Outline each uninfected red blood cell.
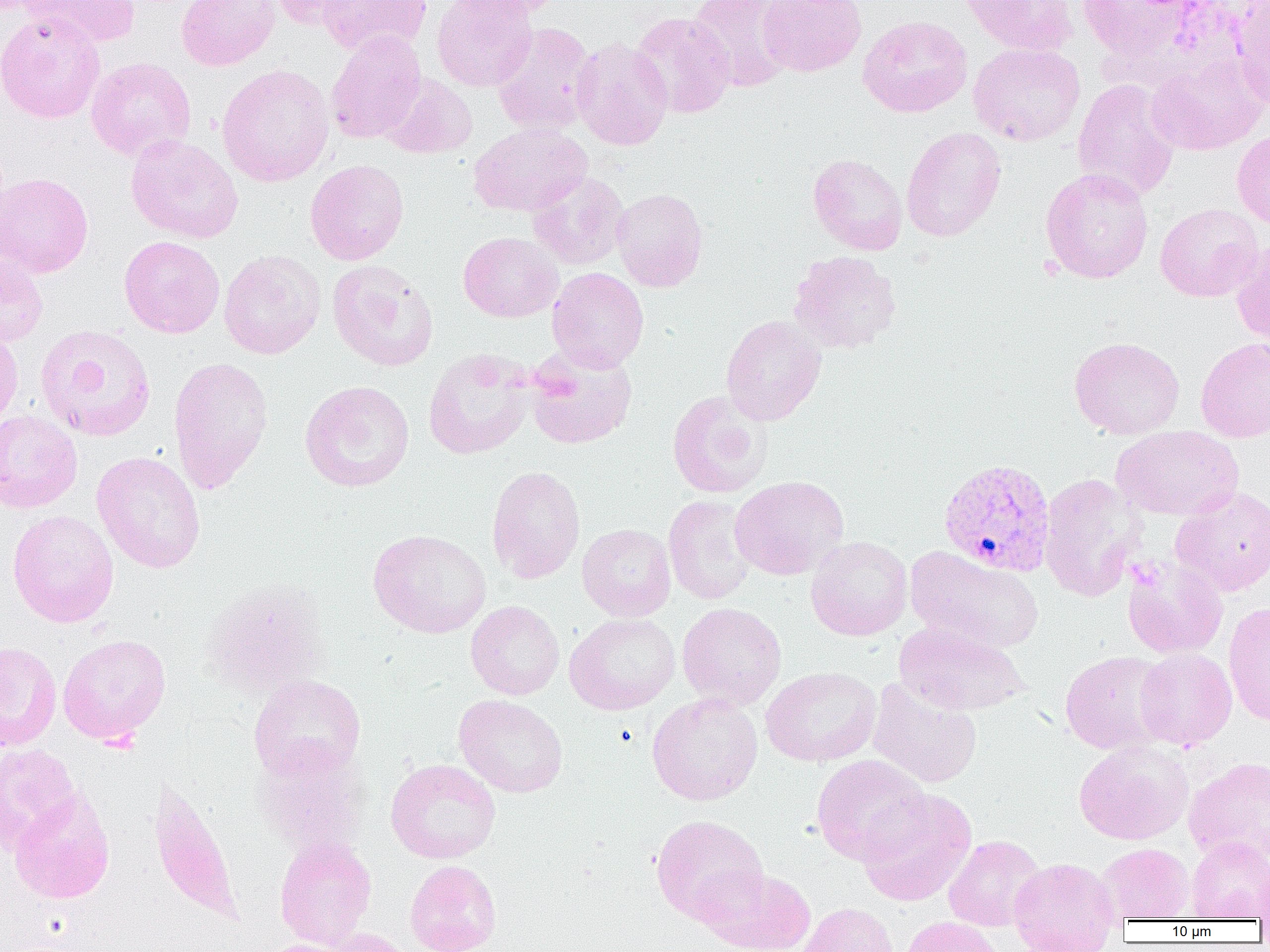
Approximate bounding boxes as [x1, y1, x2, y2] in pixels.
Uninfected red blood cells: [19, 0, 140, 48], [176, 0, 280, 71], [267, 0, 363, 30], [317, 0, 432, 57], [432, 0, 538, 92], [450, 0, 563, 21], [688, 0, 796, 92], [758, 0, 866, 77], [961, 0, 1077, 57], [1078, 0, 1197, 63], [1230, 1, 1270, 110], [629, 11, 736, 118], [0, 12, 106, 123], [858, 15, 973, 118], [492, 22, 597, 137], [326, 30, 426, 144], [571, 37, 673, 151], [968, 42, 1086, 146], [1145, 52, 1268, 155], [86, 57, 196, 161], [217, 64, 335, 187], [381, 73, 477, 159], [1072, 79, 1181, 201], [469, 123, 591, 216], [901, 127, 1006, 242], [1231, 128, 1270, 229], [125, 134, 244, 243], [808, 153, 908, 255], [305, 159, 409, 266], [1040, 167, 1154, 284], [527, 171, 630, 270], [0, 172, 94, 278], [611, 188, 709, 292], [1155, 203, 1264, 302], [458, 231, 563, 322], [119, 235, 225, 338], [1231, 239, 1270, 348], [0, 250, 48, 347], [219, 250, 326, 359], [788, 250, 901, 355], [327, 259, 439, 372], [547, 267, 649, 373], [720, 314, 826, 425], [0, 324, 23, 432], [34, 324, 156, 441], [1068, 336, 1185, 439], [1195, 336, 1270, 442], [526, 346, 637, 449], [422, 348, 536, 459], [168, 356, 273, 494], [299, 380, 415, 492], [666, 391, 773, 499], [0, 409, 82, 513], [1111, 427, 1243, 521], [91, 451, 206, 573], [486, 465, 586, 584], [1039, 473, 1145, 602], [730, 475, 849, 580], [1171, 486, 1270, 597], [663, 494, 758, 605], [7, 509, 119, 628], [577, 523, 676, 621], [367, 529, 492, 638], [805, 535, 913, 641], [905, 547, 1045, 654], [1122, 555, 1228, 659], [202, 580, 329, 698], [466, 600, 564, 700], [677, 602, 787, 710], [1223, 602, 1270, 725], [564, 613, 681, 715], [894, 622, 1030, 717], [58, 633, 171, 744], [0, 642, 61, 750], [1134, 648, 1237, 750], [1059, 650, 1175, 755], [761, 666, 881, 767], [248, 674, 366, 781], [868, 677, 982, 789], [646, 693, 763, 806], [453, 694, 568, 798], [1073, 741, 1194, 845], [0, 743, 81, 853], [254, 746, 369, 857], [811, 754, 930, 864], [1184, 756, 1270, 867], [385, 758, 501, 864], [148, 779, 242, 926], [856, 787, 977, 907], [10, 788, 115, 904], [650, 814, 769, 924], [943, 834, 1046, 932], [1186, 836, 1270, 921], [275, 837, 377, 950], [1097, 842, 1194, 923], [1008, 857, 1121, 951], [405, 860, 502, 952], [695, 866, 816, 952], [798, 902, 898, 952], [900, 916, 1004, 952], [321, 928, 414, 952], [256, 938, 357, 952].

Plasmodium vivax-infected red blood cell locations: [938, 459, 1055, 577]. Slide-level diagnosis: Plasmodium vivax. Captured at 1000x magnification. Thin blood film. Light microscopy. Image is 1270×952 pixels. Single field of view.